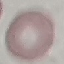 Malaria status: uninfected. Giemsa stain. Cell patch, automatically extracted from a larger field of view and resized to 64 × 64 pixels. Photographed with a smartphone camera at the microscope eyepiece. Thin blood film.